State which parasite is depicted.
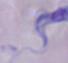

A trypanosome.

magnification = 1000x
modality = photomicrograph